Name the cell type shown.
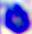
This is a leukocyte.

modality = micrograph
magnification = 400x